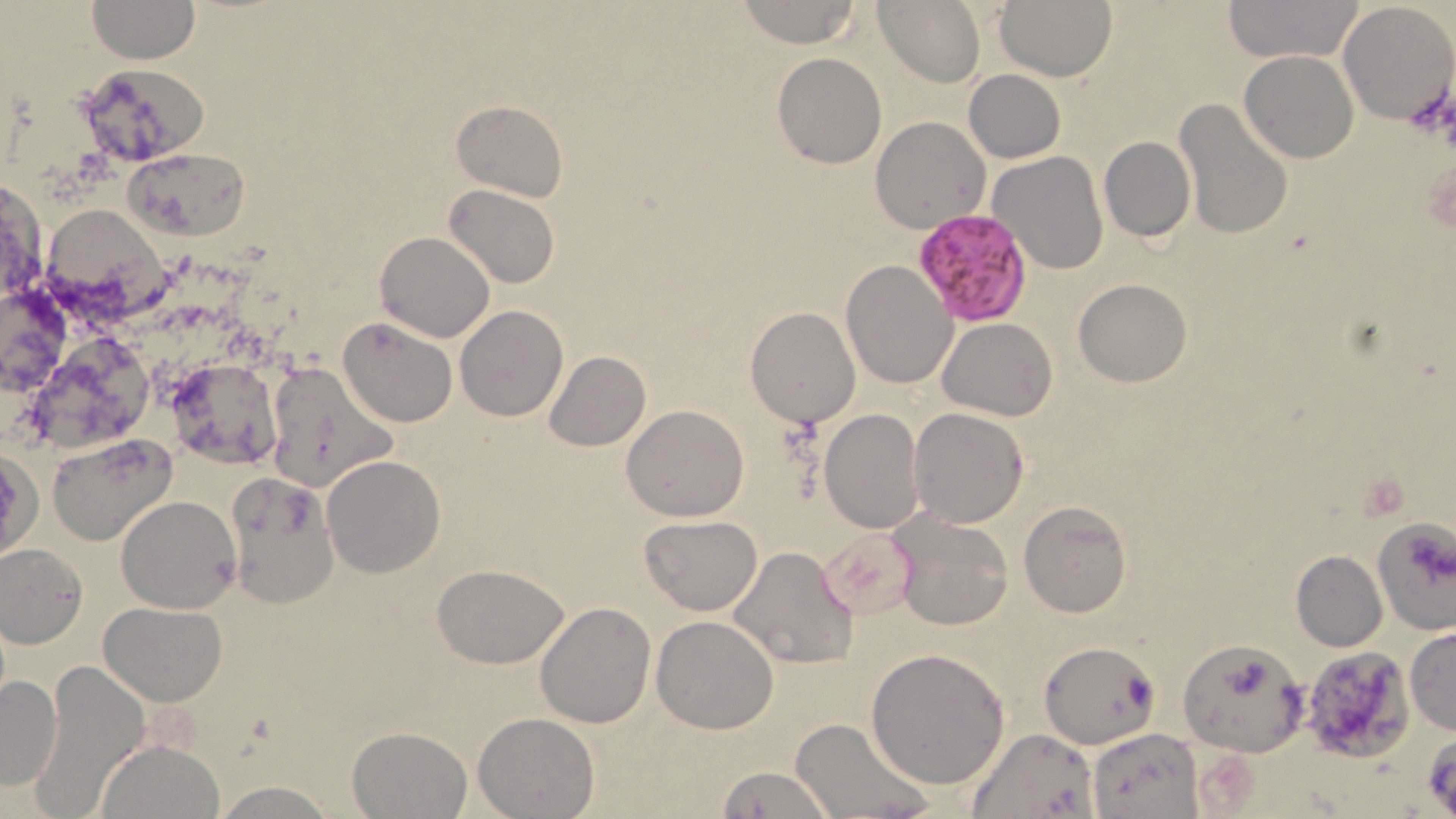 Approximate bounding boxes as (x1,y1)-(x2,y2) corner pairs in pixels. Plasmodium falciparum-infected red blood cell locations: (912,209)-(1033,325). Uninfected red blood cell locations: (87,0)-(199,63), (733,0)-(863,48), (995,0)-(1117,81), (1228,0)-(1357,62), (875,1)-(984,86), (1337,2)-(1455,123), (1240,51)-(1359,163), (772,53)-(886,168), (73,62)-(205,171), (964,69)-(1066,162), (1173,99)-(1295,243), (451,100)-(568,201), (870,116)-(990,233), (1099,137)-(1195,241), (124,146)-(250,240), (988,152)-(1109,276), (1,170)-(45,315), (444,184)-(560,288), (47,197)-(178,319), (375,230)-(495,341), (841,259)-(956,389), (1073,279)-(1192,386), (1,283)-(74,401), (455,306)-(568,421), (746,307)-(861,429), (338,316)-(459,426), (936,318)-(1056,420), (39,328)-(162,444), (543,350)-(650,451), (174,357)-(281,468), (264,358)-(395,492), (622,404)-(749,520), (819,408)-(923,533), (910,408)-(1028,528), (49,435)-(177,547), (321,455)-(446,576), (224,474)-(338,608), (115,494)-(241,613), (1018,502)-(1132,617), (889,510)-(1012,631), (640,515)-(762,614), (1373,516)-(1456,633), (0,544)-(88,647), (729,544)-(858,668), (1291,551)-(1387,651), (432,563)-(569,667), (101,602)-(226,706), (534,602)-(655,728), (651,615)-(779,733), (1405,627)-(1456,736), (1179,636)-(1307,755), (1039,640)-(1158,749), (865,647)-(1009,788), (1299,647)-(1417,764), (37,661)-(149,811), (0,675)-(62,790), (473,712)-(598,818), (790,717)-(929,819), (346,726)-(473,818), (969,726)-(1097,818), (1087,727)-(1203,819), (97,739)-(224,819), (714,765)-(835,819), (210,781)-(342,817). Slide-level diagnosis: Plasmodium falciparum. Light microscopy. May-Grünwald-Giemsa-stained preparation. Image is 1456×819 pixels. Single field of view. 1000x magnification. Thin blood smear.